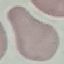
result = no malaria parasites seen
stain = Giemsa
image type = cell patch, automatically extracted from a larger field of view and resized to 64 × 64 pixels
preparation = thin smear
capture = smartphone camera at the microscope eyepiece